State which cell type is depicted.
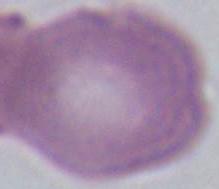
This is an erythrocyte.

Photomicrograph. 1000x magnification.